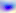 Toxoplasma gondii is shown. 400x magnification. Micrograph.